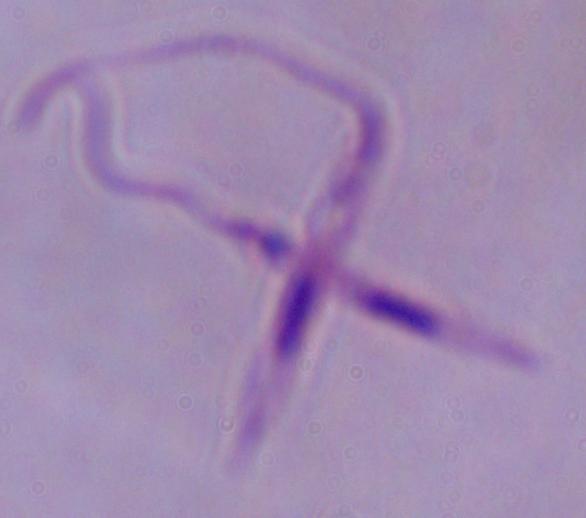

{
  "identification": "Leishmania",
  "modality": "micrograph",
  "magnification": "1000x"
}